Classify the preparation.
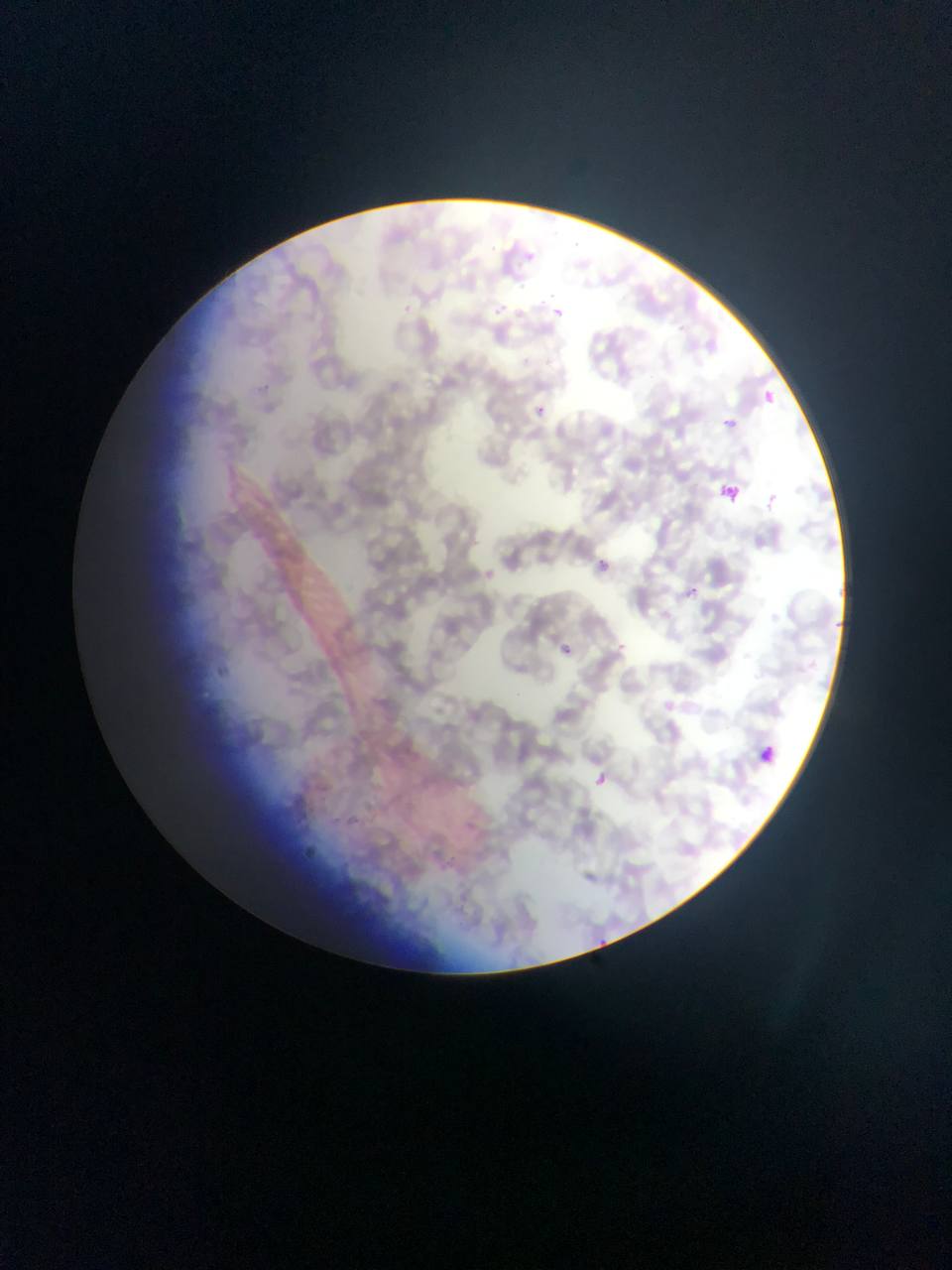
This is a thin smear.

Approximate bounding boxes as (left, top, right, bottom) in pixels.
Summary:
  - Plasmodium parasite locations: (486, 241, 506, 253), (521, 246, 544, 263), (552, 300, 575, 322), (400, 302, 421, 314), (494, 302, 517, 317), (261, 379, 276, 394), (759, 383, 782, 407), (530, 401, 557, 417), (720, 414, 739, 428), (719, 479, 744, 508), (767, 489, 781, 515), (589, 554, 615, 572), (481, 558, 499, 583), (689, 581, 703, 599), (832, 616, 845, 629), (558, 639, 579, 659), (659, 698, 681, 715), (755, 741, 781, 767), (592, 766, 613, 791), (304, 842, 320, 863), (593, 934, 610, 951)
  - Country: Ghana
  - Capture: mobile-phone photograph through a microscope
  - Field of view: single
  - Image size: 952×1270 pixels